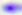
identification: Toxoplasma gondii
magnification: 400x
modality: photomicrograph